State which parasite is depicted.
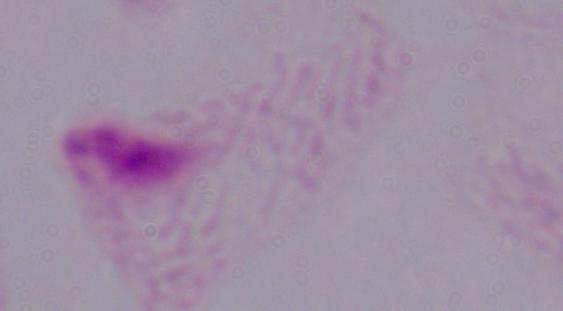
This is a trichomonad.

{
  "modality": "photomicrograph",
  "magnification": "1000x"
}